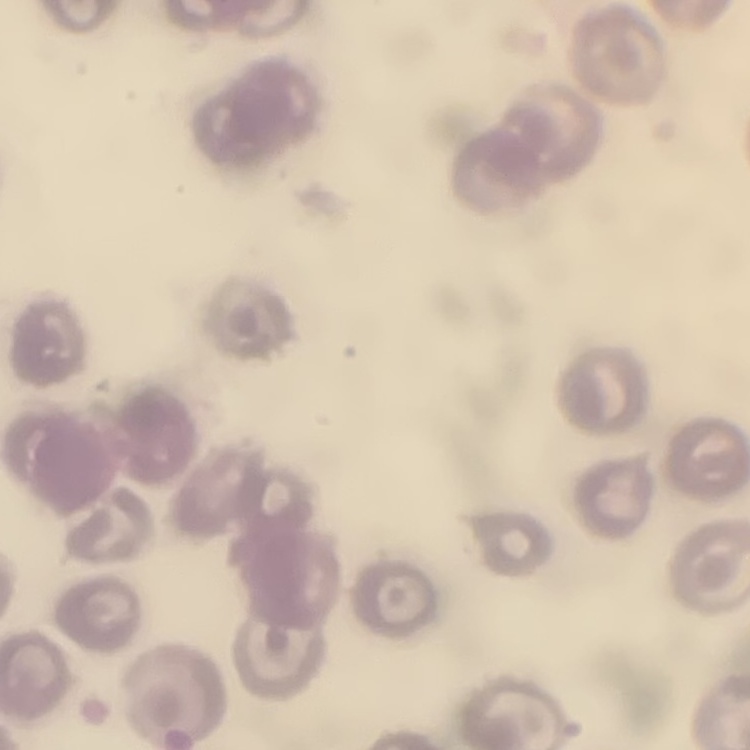 The erythrocytes exhibit no rouleaux formation. Stained with either Field's or Giemsa. Thin peripheral smear. Square crop of a larger photomicrograph.